Name the parasite shown.
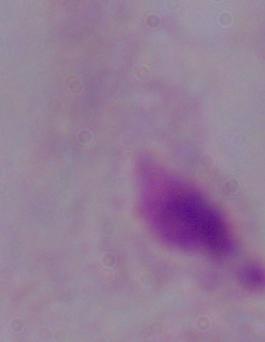

A trichomonad.

1000x magnification. Micrograph.